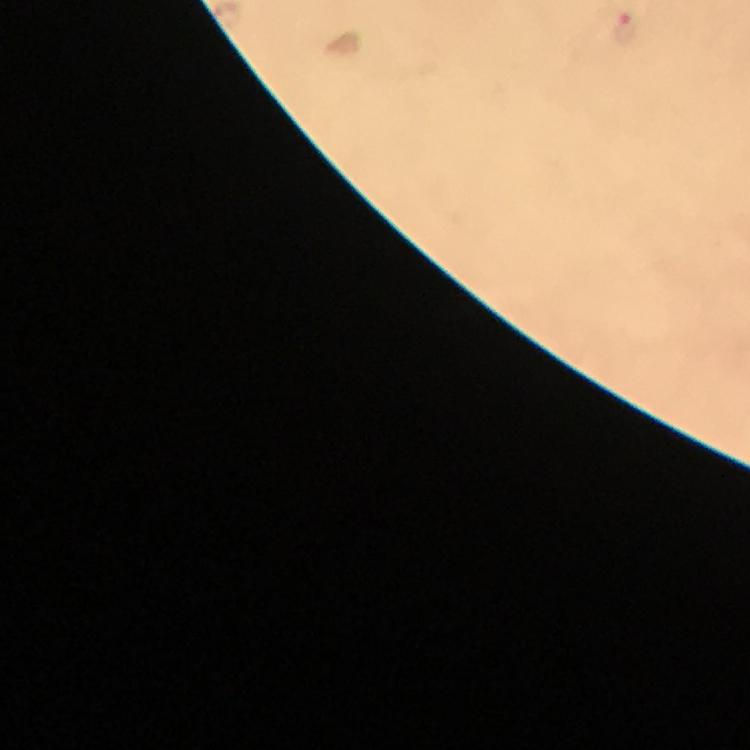
Approximate centers as {x, y} in pixels.
Summary:
  - Plasmodium parasite locations: {626, 25}
  - Preparation: thick blood film
  - Immersion oil: applied
  - Cropped from: a single field of view
  - Context: from a diagnostic examination for malaria
  - Capture: smartphone photograph through a microscope
  - Magnification: 100x
  - Stain: Giemsa
  - Image size: 750×750 pixels